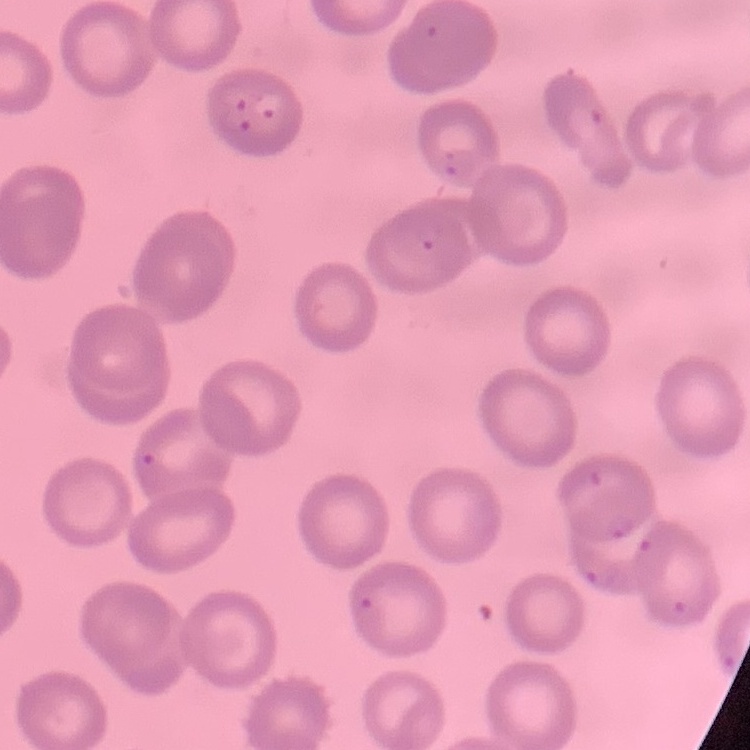

The erythrocytes show no rouleaux formation. One tile cut from a larger photomicrograph. Thin peripheral smear. Field's or Giemsa stain.